Outline each blood parasite and name the species.
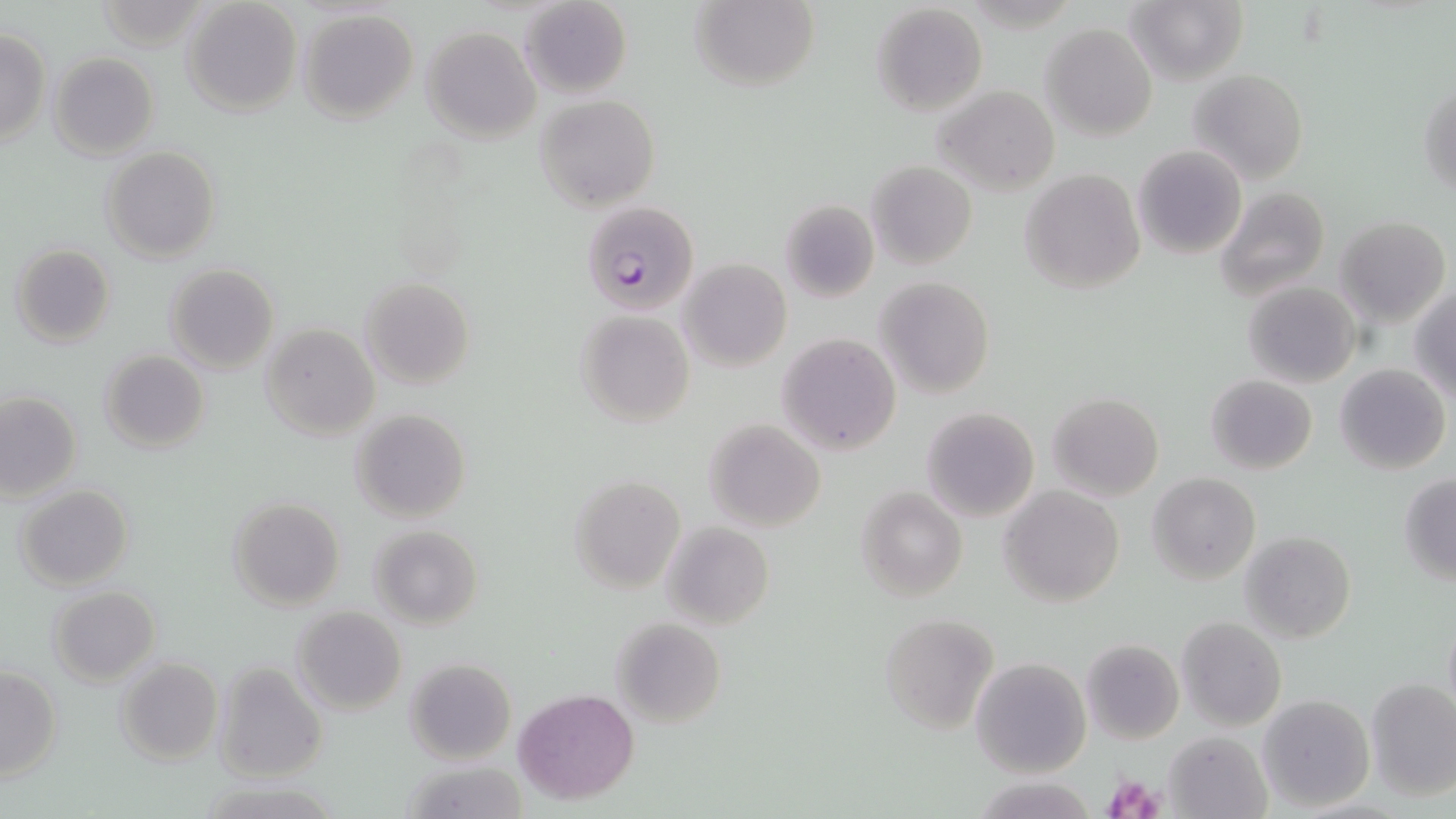
Approximate bounding boxes as (x1,y1)-(x2,y2) corner pairs in pixels.
Plasmodium falciparum-infected red blood cells: (582,200)-(699,316).
No Plasmodium ovale, Plasmodium malariae, Plasmodium vivax, Babesia divergens, or Trypanosoma brucei observed.

slide_level_diagnosis: Plasmodium falciparum
modality: light microscopy
image_size: 1456×819 pixels
field_of_view: single
stain: May-Grünwald-Giemsa
magnification: 1000x
platelet_locations: 'approximate bounding boxes as (x1,y1)-(x2,y2) corner pairs in pixels: (1102,772)-(1163,818)'
preparation: thin blood film
uninfected_red_blood_cell_locations: 'approximate bounding boxes as (x1,y1)-(x2,y2) corner pairs in pixels: (692,0)-(820,92), (1126,0)-(1247,85), (519,1)-(631,98), (182,2)-(301,117), (870,3)-(988,116), (299,9)-(419,124), (1042,22)-(1158,139), (422,27)-(540,142), (0,29)-(51,147), (48,52)-(161,160), (1189,69)-(1309,185), (1419,77)-(1455,199), (935,87)-(1058,194), (536,95)-(660,210), (102,145)-(220,264), (1134,146)-(1246,260), (867,159)-(977,270), (1019,169)-(1145,295), (1213,186)-(1330,300), (779,198)-(880,303), (1337,216)-(1450,327), (10,245)-(115,347), (679,259)-(791,371), (166,264)-(278,374), (874,275)-(994,399), (359,277)-(475,389), (1243,280)-(1360,388), (1410,288)-(1456,402), (575,310)-(695,426), (260,324)-(379,439), (777,333)-(902,454), (100,349)-(210,453), (1334,363)-(1451,476), (1206,374)-(1317,474), (1048,392)-(1163,500), (0,393)-(83,502), (920,407)-(1040,523), (351,409)-(471,524), (704,420)-(826,533), (1148,472)-(1260,586), (568,473)-(686,592), (1399,475)-(1456,585), (15,483)-(134,590), (856,484)-(968,602), (1000,485)-(1125,606), (229,497)-(345,610), (662,521)-(773,630), (370,525)-(483,629), (1240,532)-(1356,643), (49,586)-(159,685), (292,607)-(407,716), (1442,612)-(1456,722), (877,613)-(997,734), (1177,617)-(1286,730), (611,618)-(726,730), (1080,638)-(1185,746), (970,655)-(1091,777), (115,656)-(223,765), (406,659)-(516,765), (214,661)-(328,783), (0,666)-(61,781), (1365,678)-(1456,800), (513,689)-(638,803), (1256,693)-(1375,814), (1165,730)-(1271,817), (399,762)-(528,817)'